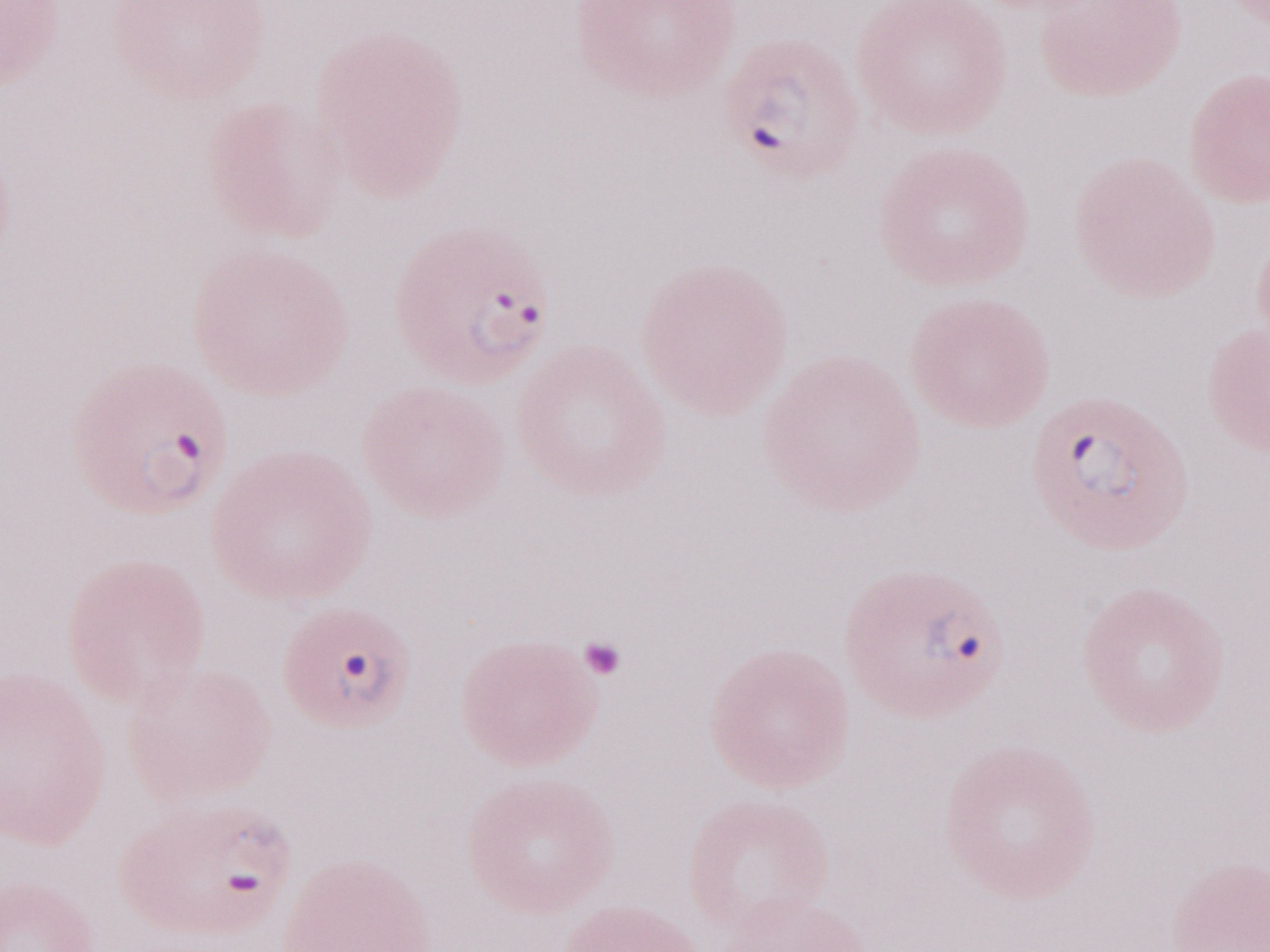 Image is 1270×952 pixels. Malaria diagnosis (patient-level): positive. 1,000x magnification. May-Grünwald-Giemsa-stained preparation. One field of this slide. Thin peripheral-blood smear. Olympus BX43 microscope and DP73 digital camera.